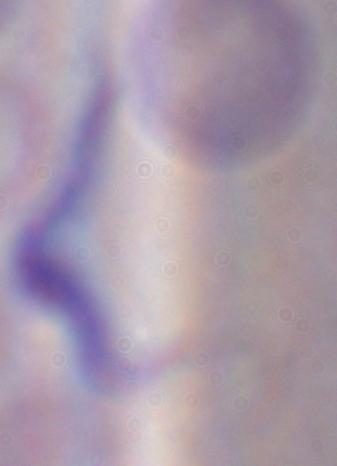
modality = photomicrograph
identification = trypanosome
magnification = 1000x